Point out each malaria parasite and each leukocyte.
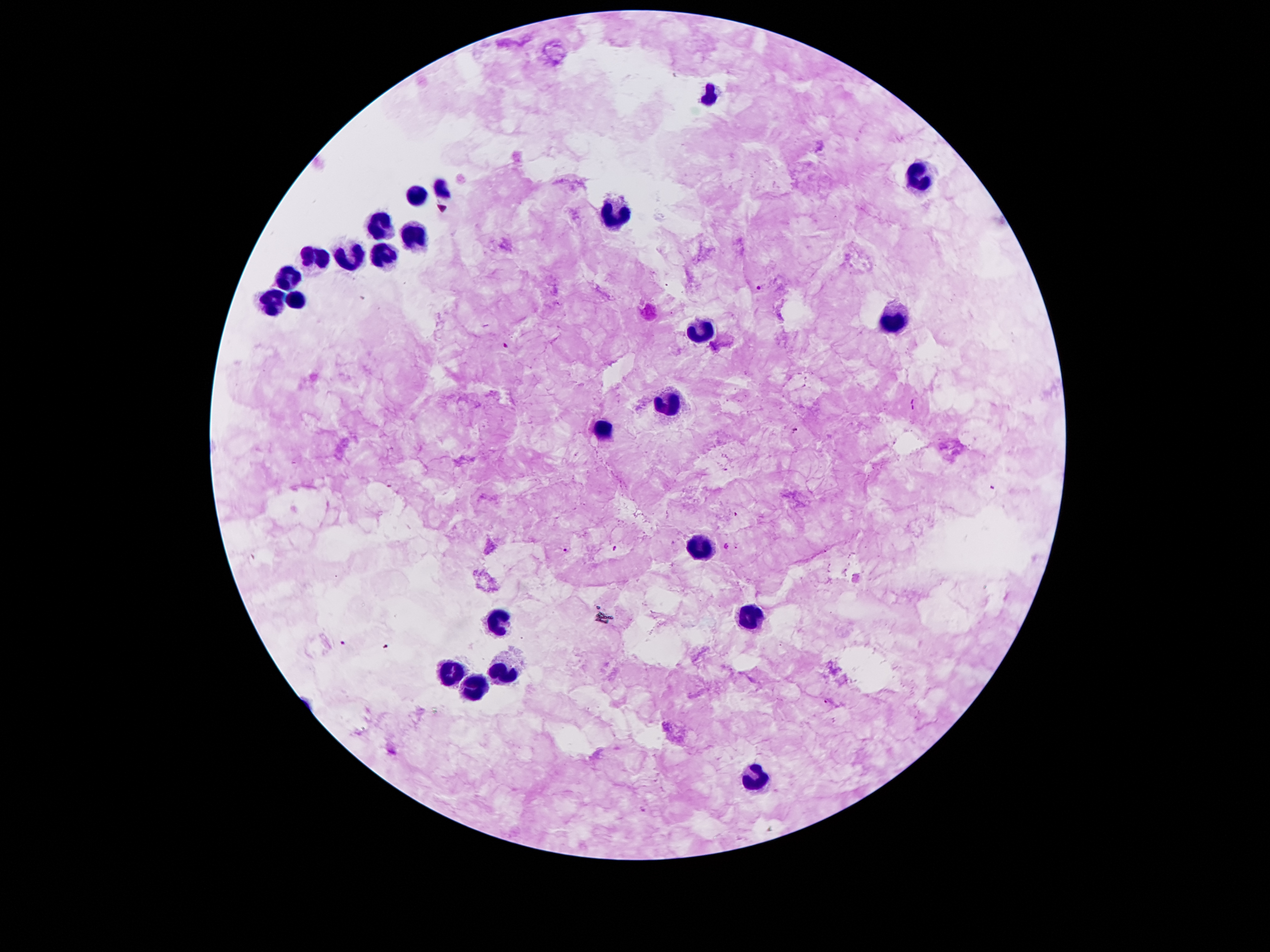

Approximate centers as (x, y) in pixels.
Malaria parasites: (757, 287), (505, 346), (794, 431), (992, 488), (614, 548), (566, 550), (344, 642), (825, 701).
Leukocytes: (713, 92), (918, 177), (440, 191), (414, 197), (615, 215), (377, 224), (416, 237), (384, 252), (316, 258), (352, 264), (289, 279), (296, 296), (272, 299), (893, 320), (697, 334), (669, 404), (601, 430), (701, 545), (746, 615), (500, 617), (505, 671), (452, 673), (475, 687), (753, 776).

Giemsa stain. Thick peripheral-blood smear. 100x magnification. Image is 1270×952 pixels. Photographed through the microscope eyepiece with a smartphone camera. Patient malaria status: infected with Plasmodium falciparum. One field from this slide.